Identify the parasite.
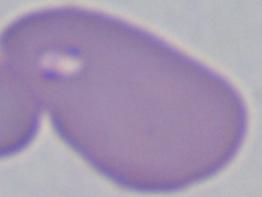

This is Babesia.

Captured at 1000x magnification. Micrograph.